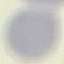

malaria_status: uninfected
capture: smartphone camera at the microscope eyepiece
image_type: cell patch, automatically extracted from a larger field of view and resized to 64 × 64 pixels
stain: Giemsa
preparation: thin smear